Classify this cell by malaria status.
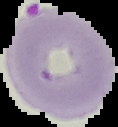
It is parasitized.

Segmented cell region on a black background. From a thin blood smear. Image is 118×127 pixels.